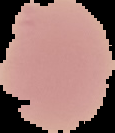

{
  "image_type": "segmented cell region with the area outside set to black",
  "preparation": "thin blood smear",
  "malaria_status": "uninfected",
  "image_size": "115×133 pixels"
}